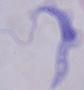

magnification = 1000x
modality = micrograph
identification = trypanosome